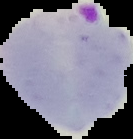
Summary:
  - Image type: segmented cell region on a black background
  - Preparation: thin blood film
  - Image size: 133×139 pixels
  - Malaria status: parasitized